State the blood parasite species.
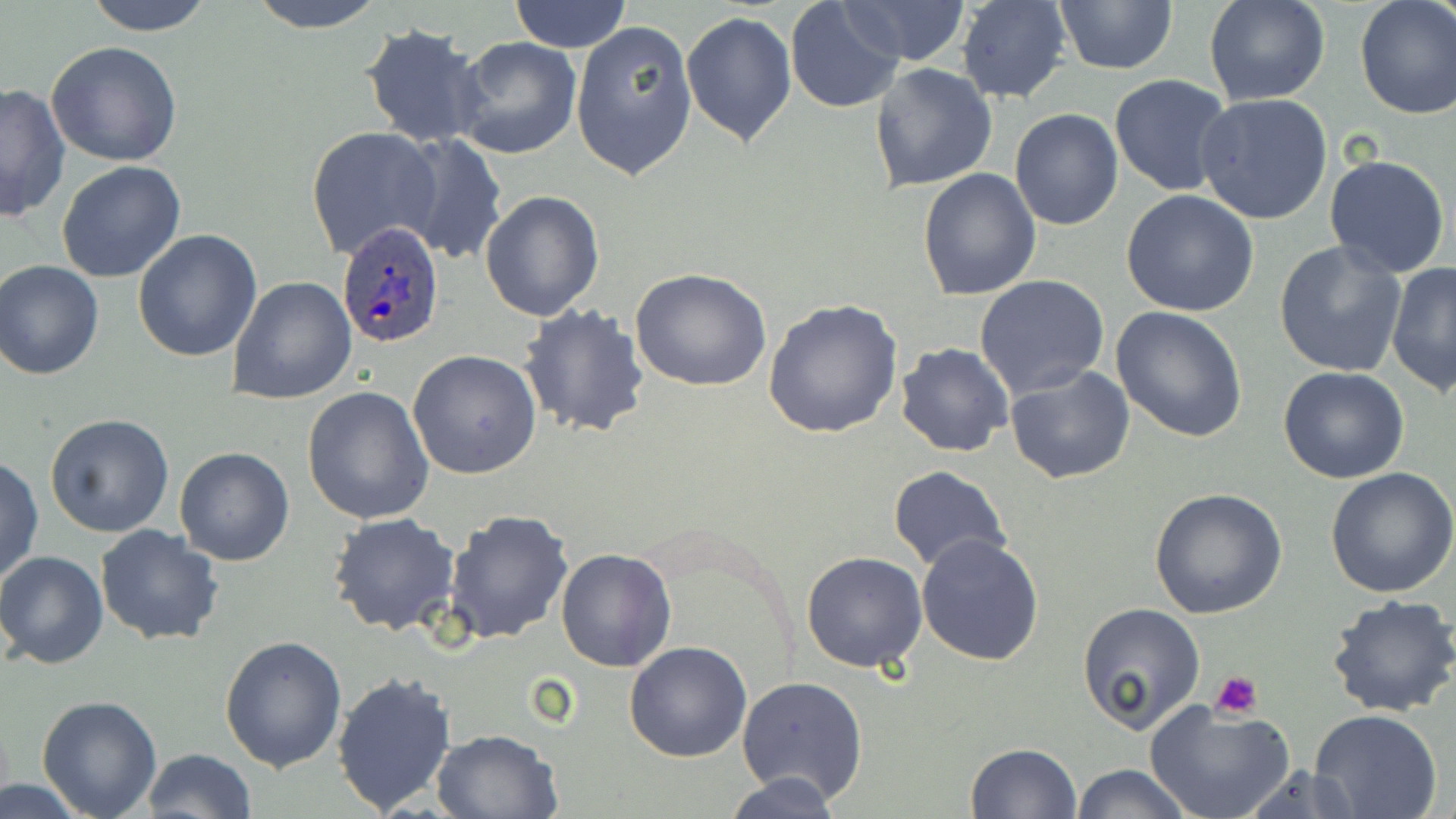

Plasmodium ovale.

Approximate bounding boxes as (x1,y1)-(x2,y2) corner pairs in pixels. Uninfected red blood cell locations: (83,0)-(217,36), (245,0)-(389,33), (510,0)-(631,53), (834,0)-(973,65), (956,0)-(1073,104), (1202,0)-(1330,106), (1354,0)-(1456,121), (783,1)-(906,115), (1053,2)-(1178,75), (680,10)-(797,146), (570,20)-(697,181), (361,24)-(489,147), (453,36)-(582,159), (44,41)-(184,168), (869,62)-(998,194), (1110,75)-(1236,196), (0,82)-(72,222), (1195,94)-(1334,226), (1010,108)-(1123,229), (306,126)-(440,260), (396,134)-(507,263), (1324,152)-(1451,279), (57,160)-(186,282), (916,167)-(1041,301), (479,190)-(603,322), (1119,190)-(1262,317), (132,229)-(262,361), (1273,240)-(1406,380), (0,260)-(105,380), (1387,260)-(1456,396), (630,268)-(772,392), (974,274)-(1110,399), (227,276)-(357,404), (763,299)-(903,439), (518,304)-(650,439), (1110,306)-(1248,443), (895,342)-(1015,458), (408,349)-(542,480), (1006,364)-(1135,485), (1277,366)-(1409,484), (302,385)-(434,524), (44,414)-(175,538), (175,446)-(294,567), (1,456)-(44,587), (887,465)-(1009,571), (1326,466)-(1456,597), (1147,488)-(1287,619), (441,508)-(575,646), (327,512)-(461,637), (94,524)-(223,645), (914,531)-(1045,667), (554,547)-(676,671), (0,550)-(109,670), (800,552)-(929,673), (1325,593)-(1456,718), (1077,603)-(1206,736), (220,635)-(347,773), (623,641)-(752,762), (330,671)-(457,817), (736,675)-(869,805), (37,696)-(163,817), (1144,700)-(1297,819), (1308,710)-(1443,819), (430,728)-(562,818), (964,742)-(1083,818), (142,748)-(255,819), (1069,763)-(1195,819), (725,771)-(844,819), (1,776)-(94,818). Platelet locations: (1211,672)-(1262,719). Plasmodium ovale-infected red blood cell locations: (335,220)-(444,351). Image is 1456×819 pixels. May-Grünwald-Giemsa stain. Thin blood smear. One field of a larger specimen. Optical microscopy. Captured at 1000x magnification.